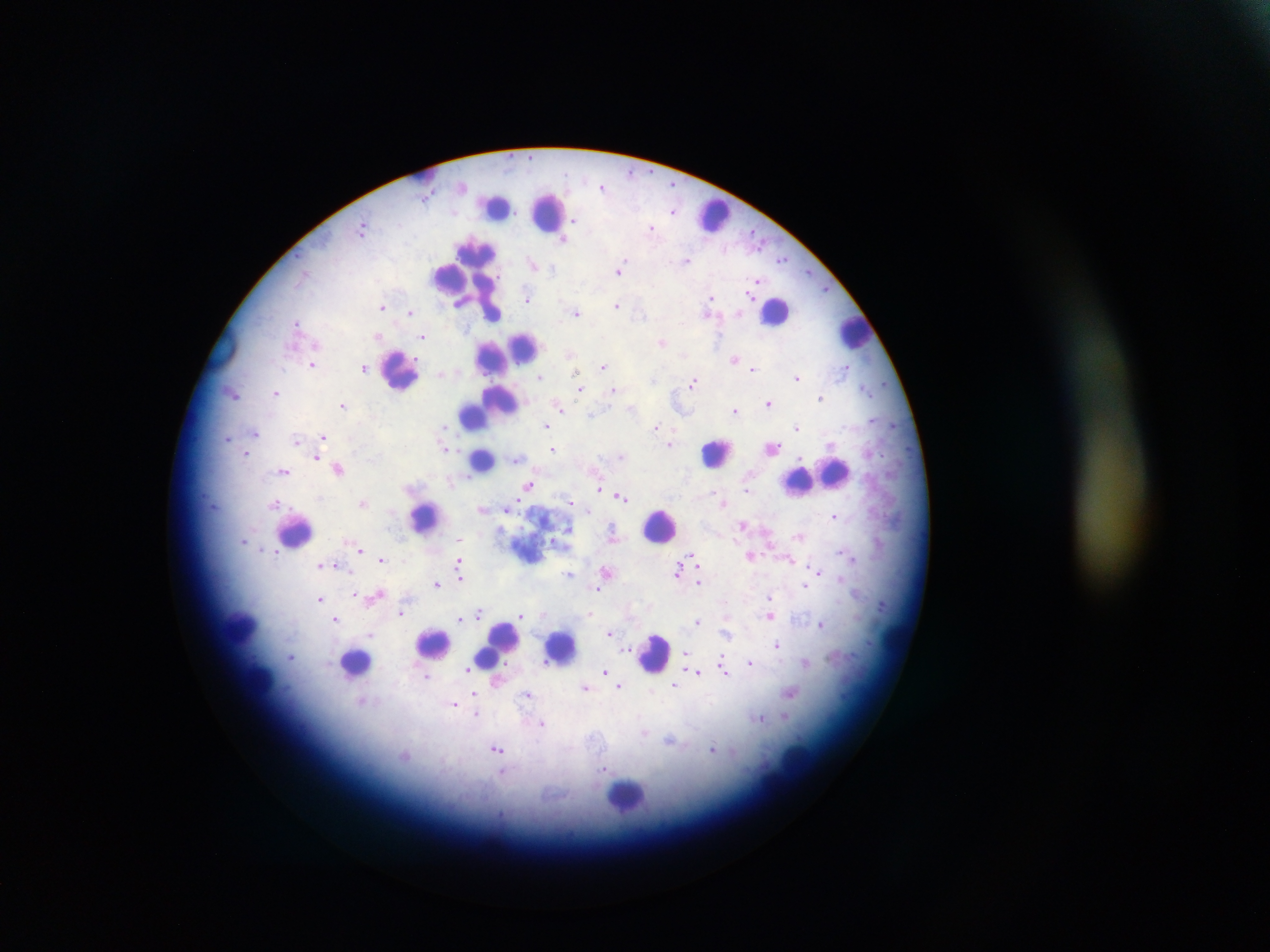
{
  "image_size": "1270×952 pixels",
  "malaria_parasite_locations": "approximate centers as (x, y) in pixels: (602, 187), (673, 211), (576, 219), (652, 227), (363, 229), (564, 238), (783, 258), (687, 260), (533, 263), (620, 269), (809, 271), (758, 281), (827, 289), (751, 295), (527, 297), (712, 298), (617, 305), (383, 306), (576, 311), (410, 312), (711, 312), (739, 313), (297, 323), (378, 336), (423, 336), (663, 342), (571, 352), (734, 358), (313, 363), (604, 366), (847, 367), (364, 368), (753, 368), (577, 371), (440, 375), (797, 375), (540, 378), (693, 382), (864, 387), (580, 388), (615, 389), (276, 392), (234, 394), (821, 397), (768, 402), (343, 405), (559, 406), (632, 408), (736, 409), (591, 415), (893, 423), (545, 425), (656, 427), (797, 427), (256, 432), (323, 437), (228, 438), (297, 439), (670, 444), (772, 446), (445, 447), (553, 448), (246, 453), (622, 455), (316, 456), (518, 458), (339, 467), (284, 471), (529, 485), (599, 487), (748, 487), (621, 496), (362, 502), (274, 503), (571, 503), (725, 503), (577, 505), (483, 508), (506, 508), (834, 515), (743, 524), (569, 529), (613, 535), (799, 535), (460, 538), (244, 541), (361, 550), (692, 555), (751, 555), (853, 557), (382, 559), (791, 561), (328, 564), (459, 564), (321, 565), (336, 565), (678, 570), (818, 570), (607, 571), (569, 573), (461, 578), (699, 582), (437, 584), (805, 584), (597, 590), (354, 593), (375, 595), (320, 598), (769, 598), (882, 604), (401, 613), (542, 613), (591, 614), (521, 615), (481, 616), (772, 616), (336, 618), (460, 618), (698, 622), (822, 624), (610, 633), (728, 633), (371, 635), (777, 645), (686, 654), (291, 655), (544, 662), (751, 662), (805, 662), (722, 663), (467, 670), (697, 671), (724, 671), (606, 672), (426, 676), (497, 679), (675, 685), (586, 686), (620, 686), (791, 694), (474, 695), (528, 695), (363, 701), (454, 703), (783, 716), (758, 718), (543, 723), (671, 740), (712, 749), (498, 750), (405, 756), (606, 768)",
  "field_of_view": "single",
  "country": "Ghana",
  "capture": "mobile-phone photograph through a microscope",
  "leukocyte_locations": "approximate centers as (x, y) in pixels: (497, 207), (548, 212), (713, 216), (452, 277), (470, 277), (775, 310), (854, 331), (517, 351), (496, 357), (401, 370), (490, 405), (474, 413), (716, 453), (482, 460), (834, 472), (815, 477), (801, 480), (425, 517), (659, 525), (294, 530), (238, 626), (898, 639), (433, 643), (561, 646), (497, 647), (654, 654), (356, 663), (259, 681), (797, 763), (771, 782), (626, 796)",
  "preparation": "thick blood film"
}